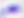
Toxoplasma gondii is seen. Micrograph. Captured at 400x magnification.